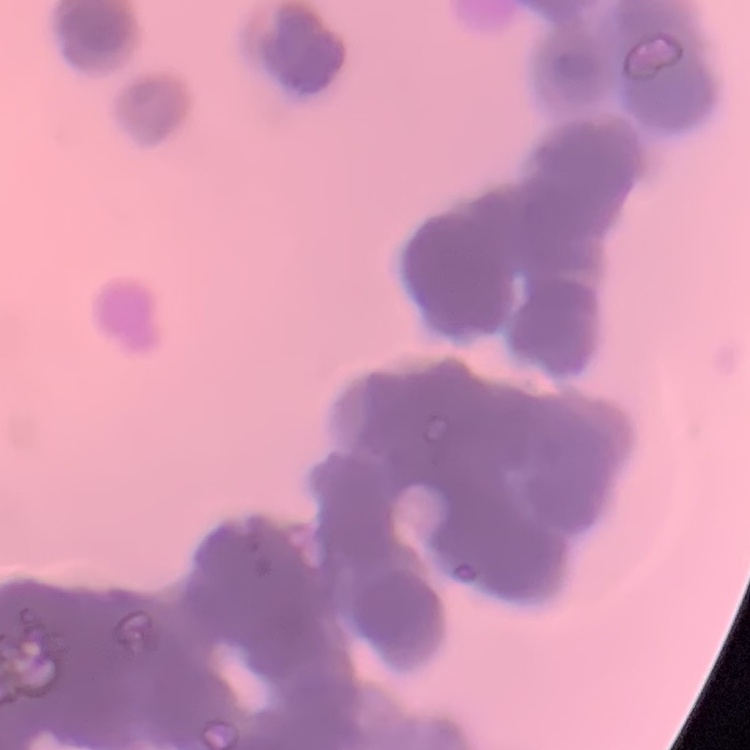 The erythrocytes show rouleaux formation. One tile cut from a larger photomicrograph. Field's or Giemsa stain. Thin blood smear.